Assess for malaria.
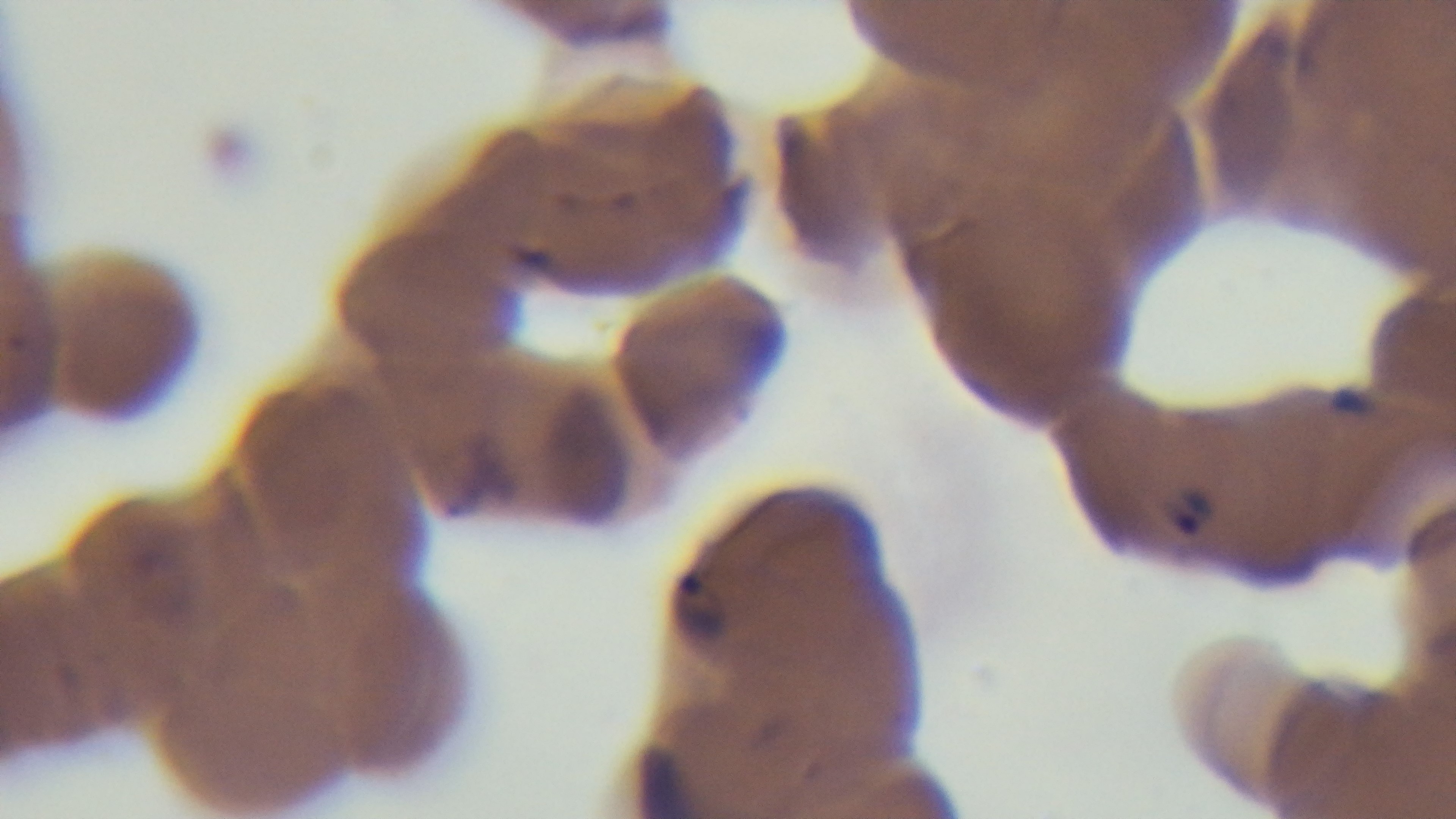

Positive.

One field from the slide. Preparation: thin. Giemsa stain. 100x oil-immersion objective. Captured with a mounted 4K digital camera. Photomicrograph.